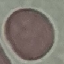
result: no malaria parasites detected
image_type: automatically extracted cell patch, resized to 64 × 64 pixels
preparation: thin blood film
capture: smartphone camera at the microscope eyepiece
stain: Giemsa